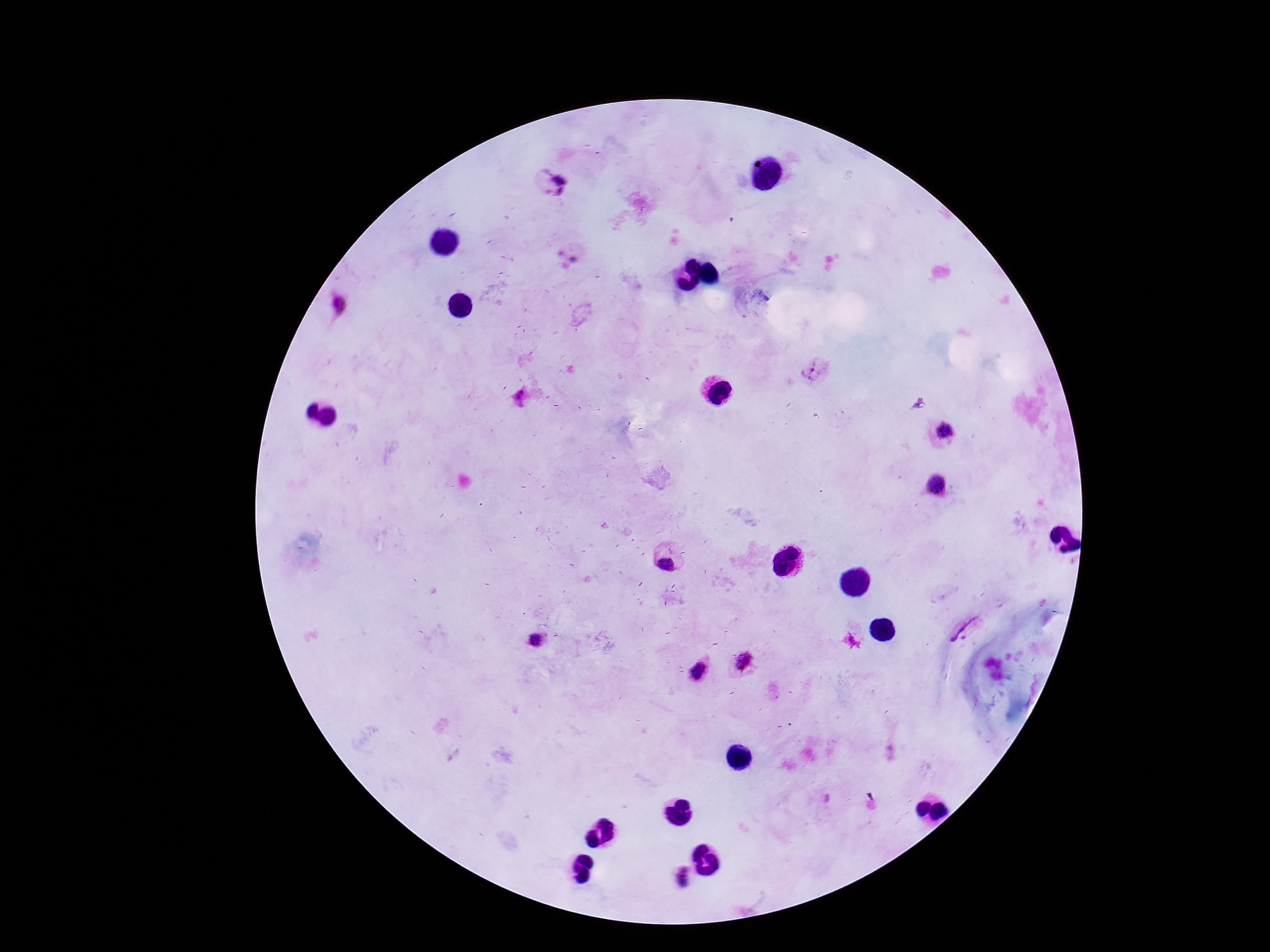 Approximate centers as [x, y] in pixels. Plasmodium parasite locations: [557, 182], [813, 369], [946, 431], [937, 485], [666, 564], [534, 640], [747, 658], [699, 670], [683, 880]. Single field of view. 100x magnification. Photographed through the microscope eyepiece with a smartphone camera. Thick peripheral-blood smear. Giemsa-stained preparation. Patient malaria status: positive. Image is 1270×952 pixels.